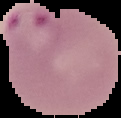

From a thin blood film. Result: Plasmodium parasites detected. Image is 121×118 pixels. The area outside the segmented cell region is set to black.